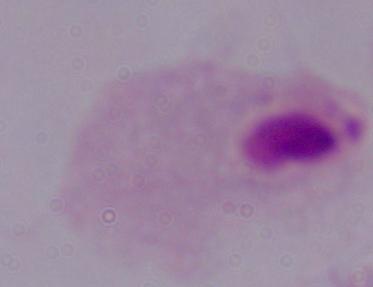
Summary:
  - Identification: trichomonad
  - Modality: micrograph
  - Magnification: 1000x